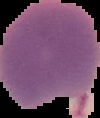

Summary:
  - Result: Plasmodium parasites identified
  - Preparation: thin blood smear
  - Image type: cell region segmented out of the field of view; surrounding area masked to black
  - Image size: 100×118 pixels